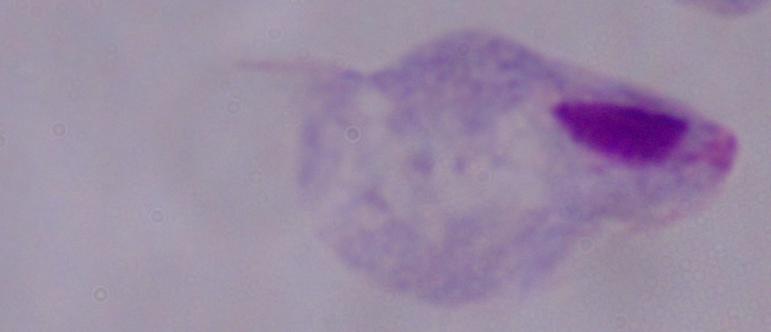
{
  "magnification": "1000x",
  "identification": "trichomonad",
  "modality": "micrograph"
}